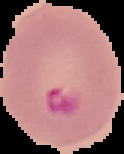
From a thin blood film. Malaria status: parasitized. The area outside the segmented cell region is set to black. Image is 124×154 pixels.